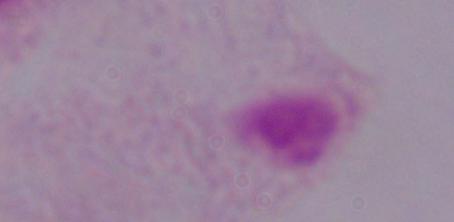
magnification: 1000x
modality: photomicrograph
identification: trichomonad